State which cell type is depicted.
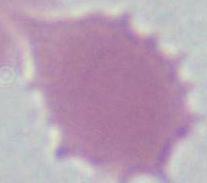
This is an erythrocyte.

modality = micrograph
magnification = 1000x